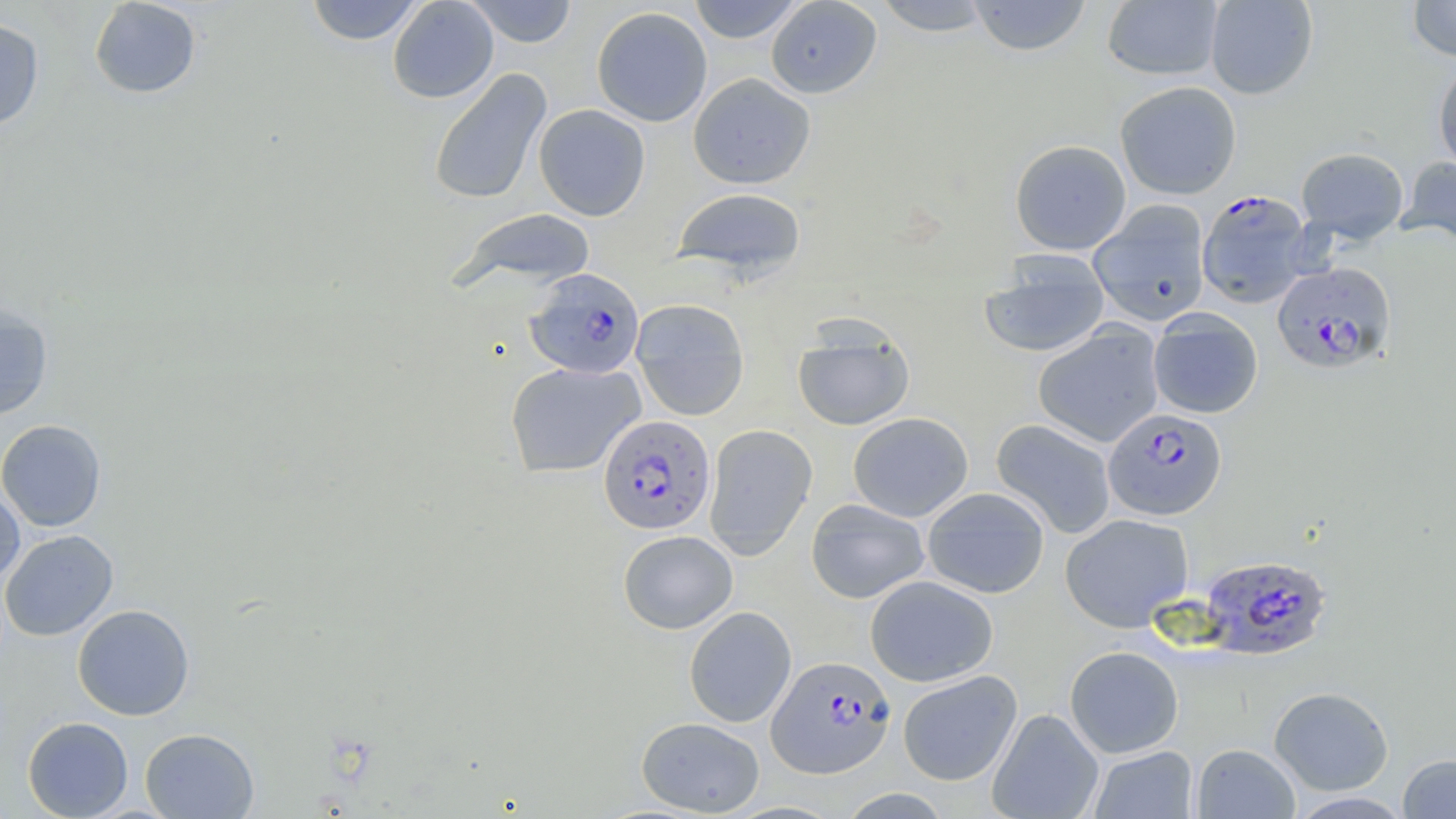

Summary:
  - Coordinate format: approximate bounding boxes as named x1/y1/x2/y2 corners in pixels
  - Plasmodium falciparum-infected red blood cell locations: (x1=1197, y1=190, x2=1312, y2=309), (x1=1271, y1=262, x2=1396, y2=373), (x1=524, y1=269, x2=645, y2=379), (x1=1103, y1=408, x2=1227, y2=520), (x1=599, y1=414, x2=716, y2=535), (x1=1199, y1=554, x2=1332, y2=661), (x1=767, y1=655, x2=895, y2=779)
  - Uninfected red blood cell locations: (x1=88, y1=0, x2=202, y2=99), (x1=305, y1=0, x2=425, y2=45), (x1=387, y1=0, x2=499, y2=103), (x1=463, y1=0, x2=580, y2=47), (x1=688, y1=0, x2=805, y2=43), (x1=765, y1=0, x2=882, y2=99), (x1=874, y1=0, x2=994, y2=36), (x1=967, y1=0, x2=1092, y2=56), (x1=1102, y1=0, x2=1224, y2=81), (x1=1204, y1=0, x2=1318, y2=99), (x1=1407, y1=0, x2=1456, y2=61), (x1=591, y1=6, x2=713, y2=127), (x1=0, y1=18, x2=45, y2=130), (x1=1433, y1=61, x2=1456, y2=174), (x1=427, y1=68, x2=552, y2=206), (x1=688, y1=72, x2=816, y2=190), (x1=1115, y1=81, x2=1242, y2=200), (x1=533, y1=104, x2=651, y2=221), (x1=1009, y1=139, x2=1131, y2=255), (x1=1296, y1=147, x2=1408, y2=243), (x1=1399, y1=156, x2=1456, y2=249), (x1=672, y1=187, x2=807, y2=280), (x1=1088, y1=200, x2=1211, y2=326), (x1=449, y1=207, x2=597, y2=295), (x1=979, y1=253, x2=1110, y2=358), (x1=630, y1=298, x2=750, y2=421), (x1=0, y1=302, x2=54, y2=420), (x1=1148, y1=309, x2=1263, y2=419), (x1=792, y1=317, x2=915, y2=432), (x1=1032, y1=324, x2=1165, y2=447), (x1=505, y1=361, x2=645, y2=478), (x1=848, y1=412, x2=973, y2=522), (x1=0, y1=419, x2=107, y2=532), (x1=990, y1=419, x2=1116, y2=539), (x1=703, y1=424, x2=817, y2=560), (x1=0, y1=483, x2=25, y2=587), (x1=922, y1=487, x2=1050, y2=599), (x1=805, y1=499, x2=930, y2=604), (x1=1060, y1=513, x2=1193, y2=632), (x1=0, y1=529, x2=118, y2=641), (x1=618, y1=530, x2=738, y2=634), (x1=865, y1=575, x2=998, y2=687), (x1=72, y1=604, x2=195, y2=721), (x1=683, y1=606, x2=796, y2=727), (x1=1064, y1=646, x2=1184, y2=758), (x1=897, y1=670, x2=1022, y2=785), (x1=1269, y1=686, x2=1394, y2=795), (x1=987, y1=708, x2=1104, y2=819), (x1=22, y1=716, x2=133, y2=818), (x1=636, y1=716, x2=765, y2=817), (x1=140, y1=728, x2=259, y2=818), (x1=1192, y1=743, x2=1300, y2=818), (x1=1089, y1=746, x2=1197, y2=818), (x1=1397, y1=753, x2=1456, y2=818), (x1=838, y1=788, x2=952, y2=818), (x1=1287, y1=791, x2=1413, y2=818)
  - Slide-level diagnosis: Plasmodium falciparum
  - Modality: light microscopy
  - Stain: May-Grünwald-Giemsa
  - Field of view: single
  - Preparation: thin blood film
  - Magnification: 1000x
  - Image size: 1456×819 pixels